Give a bounding box for every malaria parasite.
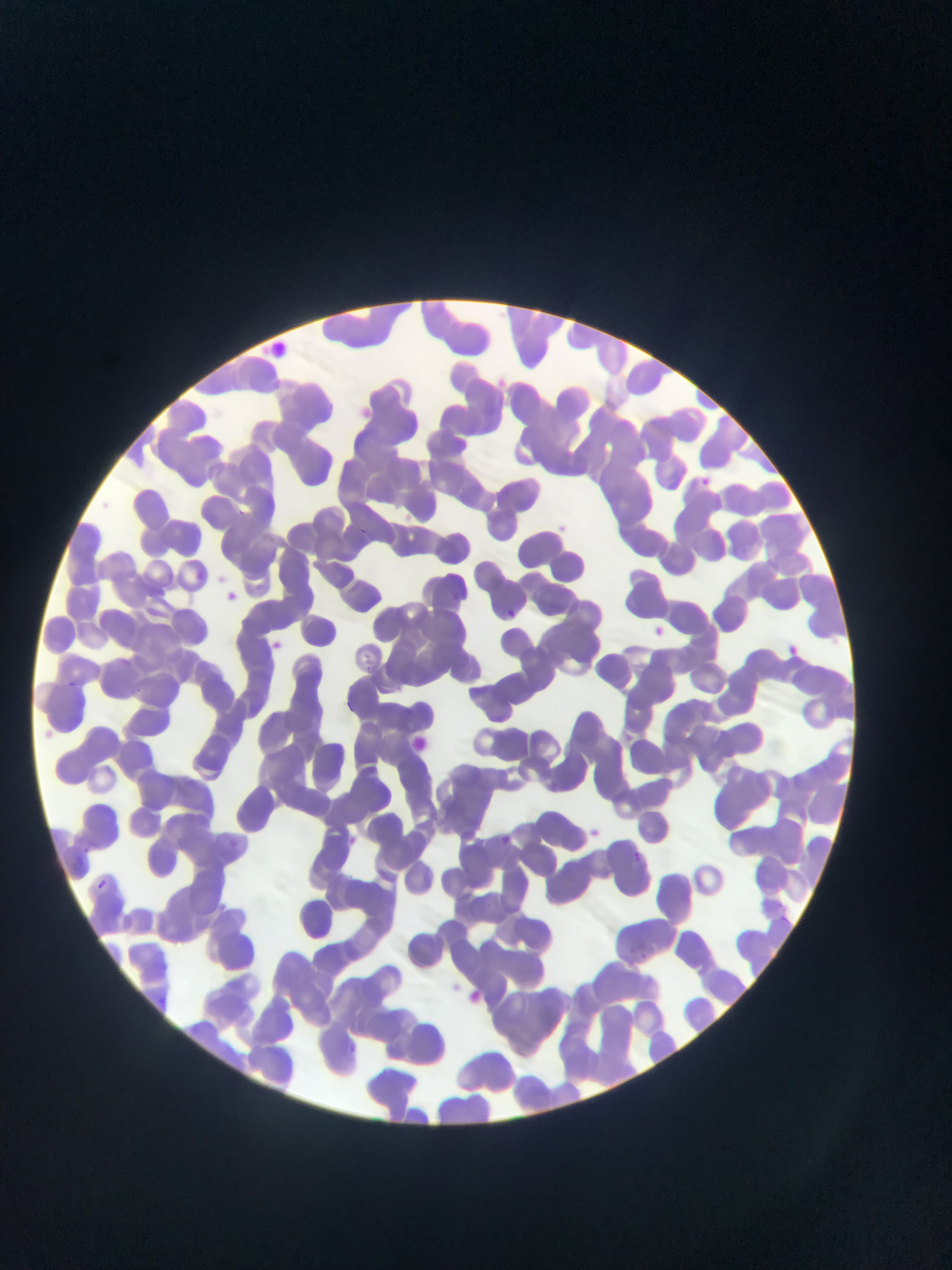

Approximate bounding boxes as [left, top, right, bottom] in pixels.
Malaria parasites: [271, 341, 288, 357], [491, 375, 512, 391], [356, 407, 373, 418], [702, 470, 716, 492], [232, 507, 255, 520], [554, 517, 570, 538], [354, 526, 377, 541], [192, 565, 209, 584], [224, 589, 241, 607], [505, 607, 519, 620], [656, 626, 666, 639], [264, 637, 282, 652], [786, 641, 803, 654], [414, 733, 431, 756], [494, 823, 517, 846], [585, 825, 604, 839], [343, 833, 363, 849], [228, 837, 239, 847], [85, 838, 94, 857], [633, 850, 643, 860], [67, 856, 91, 871], [94, 877, 113, 893], [777, 901, 795, 924], [626, 943, 651, 968], [465, 989, 487, 1003], [344, 1039, 362, 1053].

preparation: thin blood film
image_size: 952×1270 pixels
capture: mobile-phone photograph through a microscope
country: Ghana
field_of_view: single